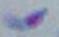
magnification = 1000x
identification = Toxoplasma gondii
modality = micrograph